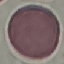

Result: no malaria parasites detected. Photographed with a smartphone camera at the microscope eyepiece. Automatically extracted cell patch, resized to 64 × 64 pixels. Giemsa stain. Thin blood film.